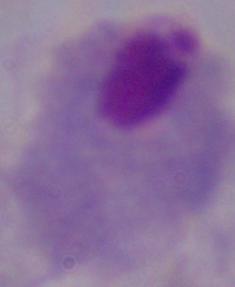
Photomicrograph. A trichomonad is shown. Captured at 1000x magnification.